State which parasite is depicted.
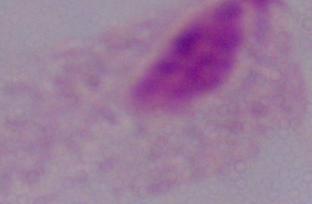
This is a trichomonad.

Photomicrograph. Captured at 1000x magnification.